Comment on the background quality.
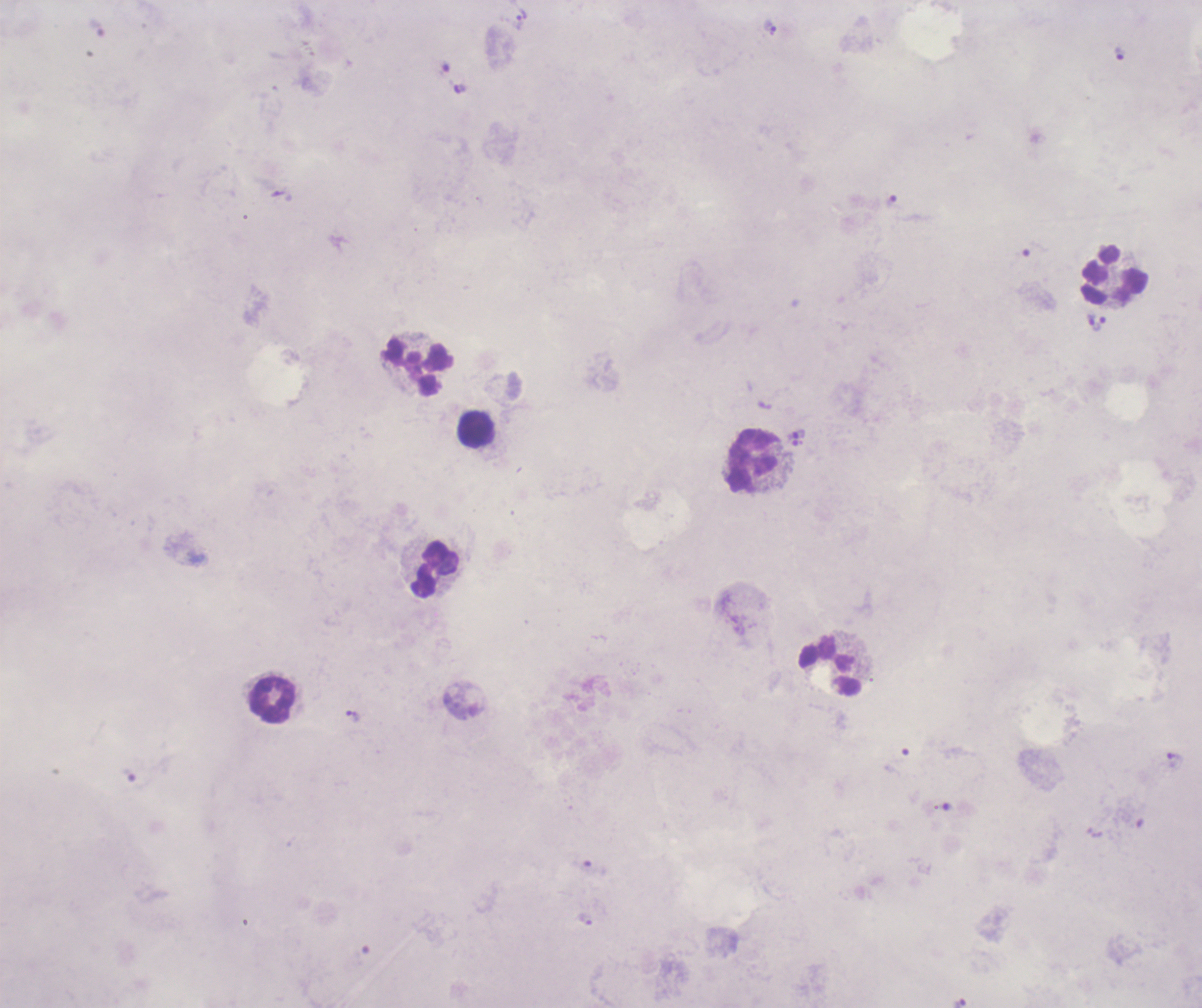

It is poor.

Approximate object centers, in pixels from the top-left corner. Trophozoite locations: (x=520, y=19), (x=770, y=27), (x=1120, y=54), (x=892, y=200), (x=1091, y=318), (x=1100, y=324), (x=796, y=434), (x=798, y=443), (x=353, y=716), (x=1175, y=760), (x=130, y=777), (x=584, y=920), (x=960, y=1003). Leukocyte locations: (x=1115, y=276), (x=418, y=368), (x=475, y=428), (x=752, y=461), (x=437, y=571), (x=830, y=668), (x=272, y=700). Image is 1202×1008 pixels. Romanowsky stain. Previously used in a real diagnosis. Captured at 100x magnification. Coloration quality: bad. Result: Plasmodium parasites identified. Thick blood smear. Single field of view.